Report the malaria status of this cell.
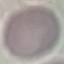

It is uninfected.

Summary:
  - Preparation: thin smear
  - Capture: smartphone camera at the microscope eyepiece
  - Stain: Giemsa
  - Image type: automatically extracted cell patch, resized to 64 × 64 pixels